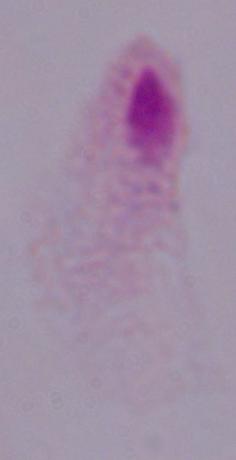

Summary:
  - Magnification: 1000x
  - Identification: trichomonad
  - Modality: photomicrograph